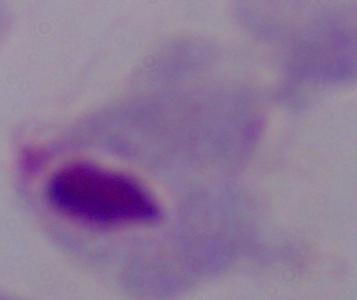 1000x magnification. A trichomonad is seen. Photomicrograph.